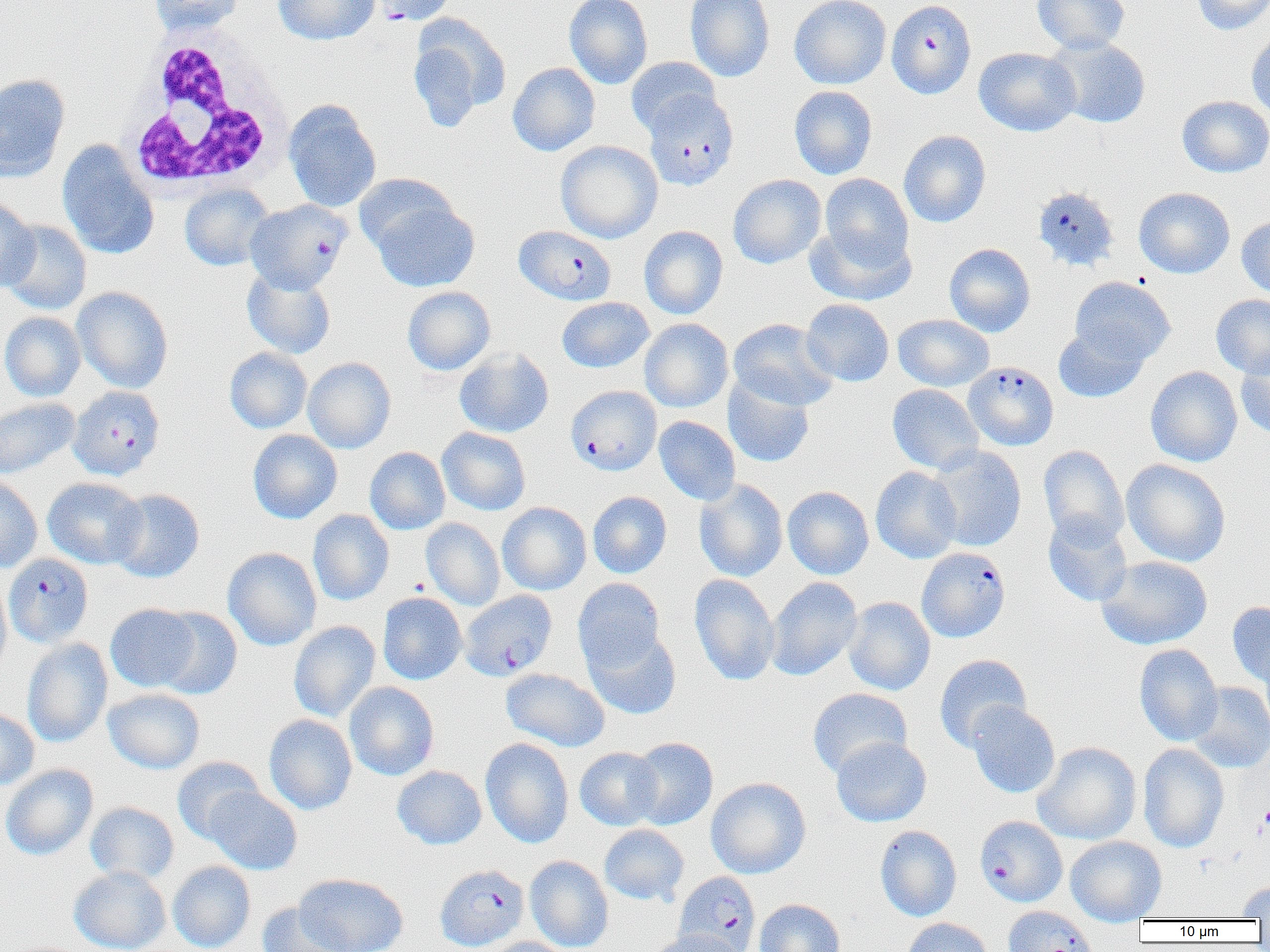

Summary:
  - Coordinate format: approximate bounding boxes as [x1, y1, x2, y2] in pixels
  - Platelet locations: [1260, 803, 1270, 834]
  - White blood cell locations: [122, 26, 292, 194]
  - Plasmodium falciparum-infected red blood cell locations (subset): [370, 0, 456, 26], [886, 1, 977, 99], [645, 91, 740, 191], [1033, 186, 1119, 272], [245, 200, 351, 293], [964, 361, 1058, 450], [566, 385, 661, 475], [71, 389, 168, 483], [916, 547, 1010, 642], [4, 553, 93, 648], [460, 590, 557, 680], [975, 816, 1067, 907], [435, 864, 528, 951], [675, 872, 760, 952]
  - Uninfected red blood cell locations (subset): [149, 0, 244, 36], [273, 0, 379, 45], [564, 0, 653, 89], [685, 0, 775, 82], [789, 0, 891, 89], [1032, 0, 1130, 54], [1191, 0, 1270, 35], [408, 14, 511, 130], [1247, 29, 1270, 121], [1045, 36, 1152, 129], [974, 47, 1081, 136], [625, 57, 721, 137], [508, 62, 600, 156], [0, 74, 70, 181], [789, 85, 877, 179], [1177, 95, 1270, 177], [283, 100, 381, 212], [899, 130, 991, 227], [57, 140, 158, 260], [555, 141, 663, 243], [354, 173, 460, 259], [820, 173, 914, 267], [728, 174, 826, 269], [180, 183, 274, 271], [1134, 187, 1235, 278], [367, 192, 480, 292], [0, 198, 38, 292], [1236, 215, 1270, 298], [1, 220, 92, 314], [805, 224, 916, 306], [639, 226, 728, 319], [945, 243, 1035, 337], [242, 268, 335, 358], [1069, 276, 1176, 366], [72, 286, 173, 393], [402, 286, 495, 375], [1211, 294, 1270, 378], [557, 297, 654, 373], [801, 299, 894, 387], [0, 311, 85, 401], [893, 314, 994, 391], [639, 318, 733, 412], [729, 318, 839, 410], [1053, 324, 1151, 404], [224, 347, 312, 433], [454, 348, 554, 438], [1235, 350, 1270, 439], [303, 357, 396, 454], [1145, 366, 1242, 467], [723, 375, 815, 468], [887, 384, 983, 474], [0, 398, 79, 479], [654, 416, 740, 505], [437, 427, 531, 515], [248, 430, 342, 524], [927, 445, 1026, 552], [1038, 445, 1128, 547], [365, 447, 450, 535], [1121, 459, 1230, 566], [871, 466, 962, 563], [0, 475, 43, 573], [43, 477, 147, 569], [695, 479, 788, 581], [783, 486, 874, 579], [109, 489, 205, 582], [588, 491, 672, 578], [497, 502, 591, 595], [308, 510, 394, 606], [1043, 514, 1133, 607], [421, 518, 504, 610], [223, 547, 322, 650], [1096, 555, 1213, 649], [690, 574, 780, 686], [0, 576, 11, 677], [766, 577, 863, 681], [573, 578, 665, 672], [378, 592, 467, 685], [844, 597, 935, 696], [1227, 601, 1270, 689], [105, 604, 200, 691], [153, 607, 242, 699], [288, 621, 381, 722], [584, 629, 681, 719], [21, 638, 113, 747], [1134, 644, 1223, 746], [934, 654, 1032, 751], [501, 668, 610, 752], [344, 681, 440, 781], [1185, 682, 1270, 773], [103, 688, 205, 774], [807, 688, 913, 778], [967, 702, 1060, 798], [0, 707, 39, 791], [263, 714, 357, 814], [831, 736, 931, 827], [628, 737, 718, 830], [480, 738, 574, 847], [1032, 742, 1141, 845], [1138, 743, 1229, 853], [575, 747, 663, 830], [172, 756, 265, 842], [1, 764, 99, 860], [392, 765, 487, 849], [706, 777, 811, 879], [204, 785, 302, 875], [86, 801, 179, 884], [599, 824, 689, 906], [875, 825, 962, 922], [1066, 836, 1167, 924], [525, 855, 613, 952], [168, 861, 255, 952], [68, 865, 171, 952], [294, 873, 408, 952], [1236, 881, 1270, 918], [754, 898, 845, 952], [257, 903, 352, 952], [901, 918, 994, 952], [646, 929, 749, 952], [485, 937, 572, 952]
  - Slide-level diagnosis: Plasmodium falciparum
  - Image size: 1270×952 pixels
  - Modality: optical microscopy
  - Field of view: single
  - Preparation: thin blood film
  - Magnification: 1000x